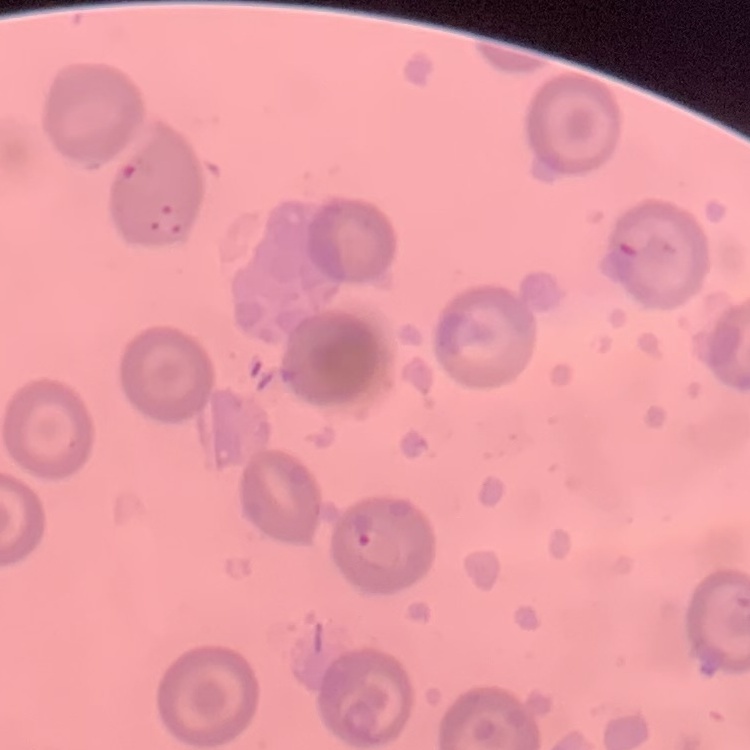 The red blood cells exhibit no rouleaux formation. Square crop of a larger photomicrograph. Stained with either Field's or Giemsa. Thin peripheral smear.